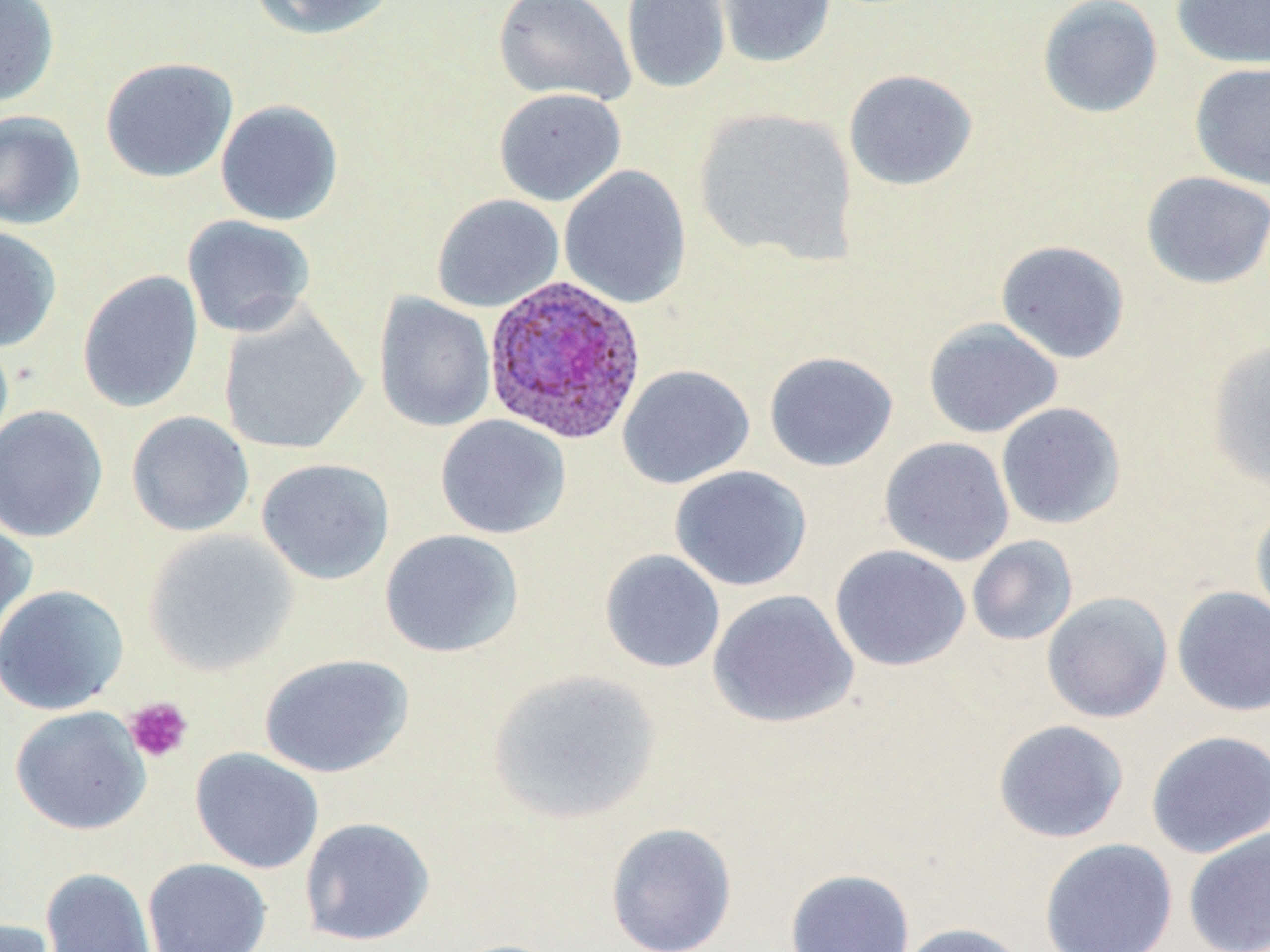
slide-level diagnosis = Plasmodium ovale
magnification = 1000x
preparation = thin blood film
Plasmodium ovale-infected red blood cell locations = approximate bounding boxes as [x1, y1, x2, y2] in pixels: [482, 274, 648, 445]
platelet locations = approximate bounding boxes as [x1, y1, x2, y2] in pixels: [124, 697, 193, 763]
image size = 1270×952 pixels
uninfected red blood cell locations = approximate bounding boxes as [x1, y1, x2, y2] in pixels: [0, 0, 59, 107], [251, 0, 398, 40], [492, 0, 635, 106], [621, 0, 731, 94], [716, 0, 836, 68], [1037, 0, 1163, 119], [1170, 0, 1270, 69], [99, 56, 238, 183], [1189, 62, 1270, 191], [843, 69, 978, 191], [493, 87, 627, 206], [215, 99, 344, 226], [693, 106, 859, 266], [0, 110, 87, 230], [559, 165, 692, 310], [1141, 171, 1270, 290], [430, 194, 564, 313], [182, 214, 316, 338], [0, 226, 62, 353], [995, 239, 1131, 364], [77, 270, 204, 412], [373, 293, 496, 433], [218, 306, 367, 456], [923, 317, 1063, 439], [0, 330, 14, 459], [1206, 339, 1270, 492], [764, 351, 898, 472], [617, 364, 754, 489], [995, 401, 1126, 530], [0, 405, 108, 542], [126, 410, 255, 537], [435, 415, 571, 539], [879, 436, 1015, 566], [256, 458, 395, 585], [669, 465, 812, 591], [1250, 502, 1270, 629], [0, 513, 36, 655], [142, 529, 299, 676], [379, 529, 524, 659], [967, 535, 1078, 646], [829, 545, 971, 671], [599, 549, 726, 674], [0, 584, 129, 715], [1171, 585, 1270, 717], [707, 589, 859, 729], [1041, 591, 1174, 723], [258, 653, 414, 778], [487, 668, 663, 825], [9, 706, 151, 836], [992, 719, 1129, 844], [1145, 730, 1270, 859], [190, 747, 325, 874], [299, 816, 435, 947], [605, 822, 738, 952], [1182, 827, 1270, 952], [1039, 838, 1178, 952], [142, 857, 273, 952], [40, 866, 159, 952], [784, 868, 916, 952], [0, 918, 63, 952], [896, 922, 1029, 952], [441, 938, 567, 952]
modality = light microscopy
stain = May-Grünwald-Giemsa
field of view = single